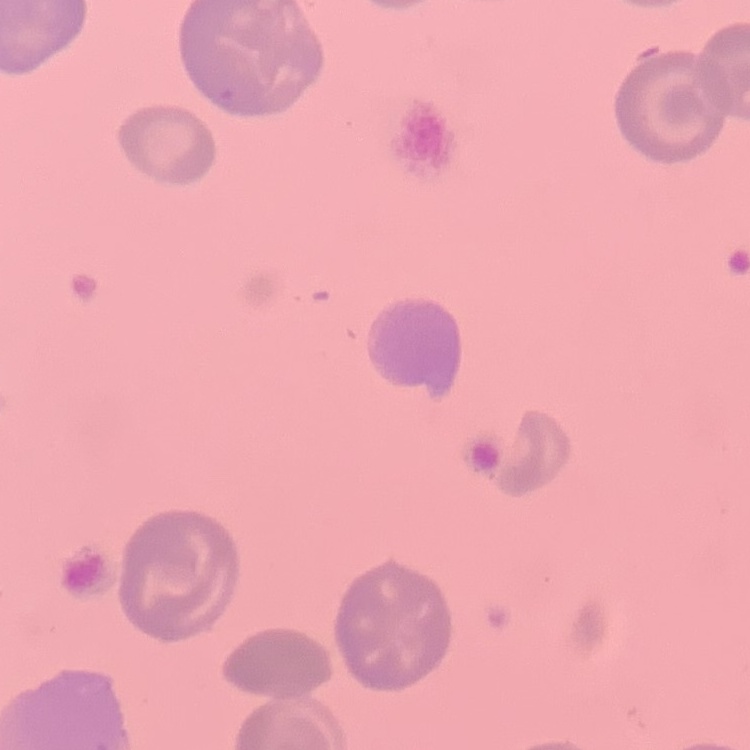
red blood cell morphology = no rouleaux formation
stain = Field's or Giemsa
image type = one tile cut from a larger photomicrograph
preparation = thin blood film